State the blood parasite species.
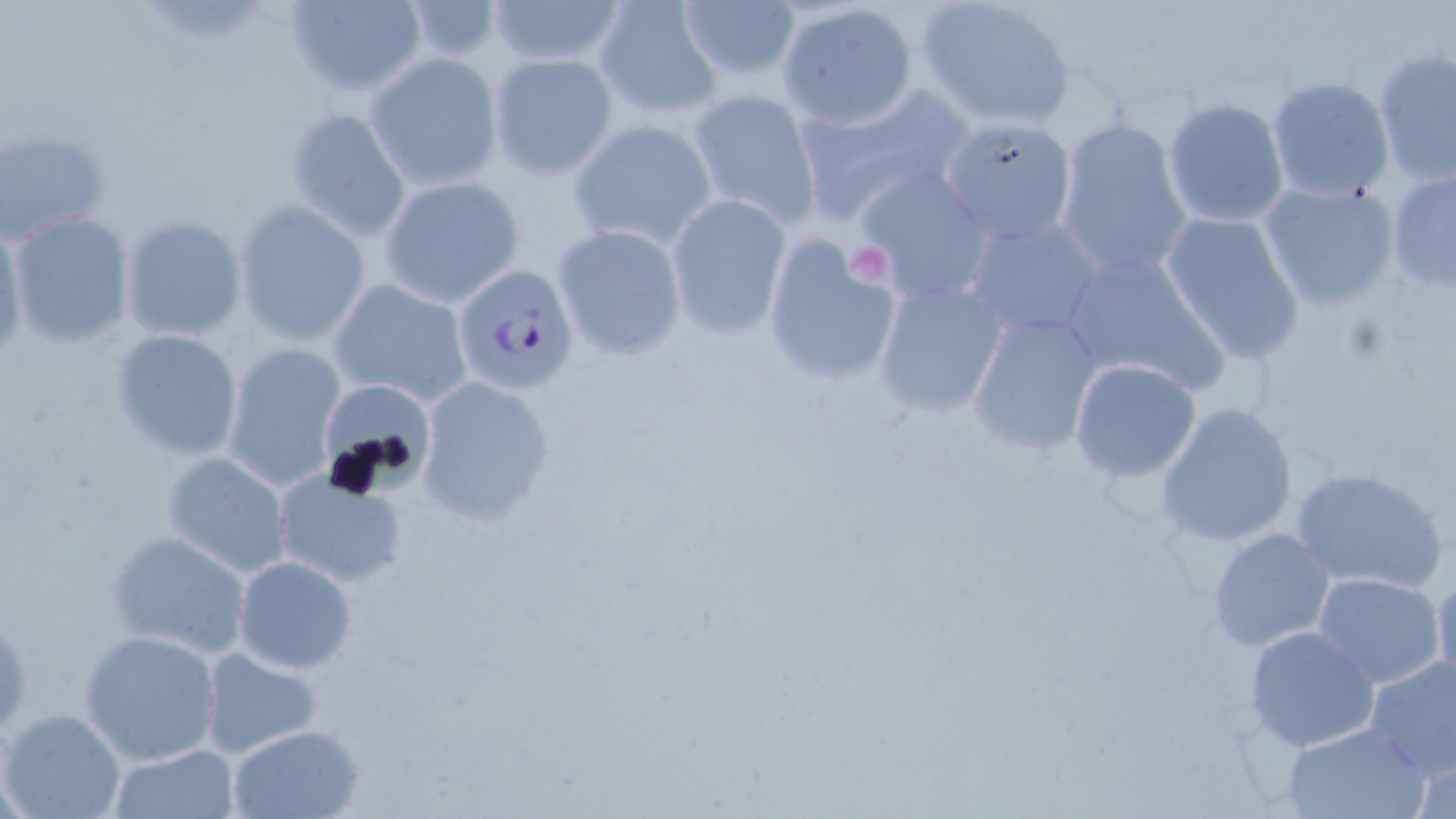

Plasmodium falciparum.

image size = 1456×819 pixels
uninfected red blood cell locations = approximate bounding boxes as [x1, y1, x2, y2] in pixels: [284, 0, 428, 99], [488, 0, 622, 69], [594, 0, 724, 121], [679, 0, 803, 84], [917, 0, 1077, 129], [401, 1, 505, 62], [778, 3, 920, 129], [1372, 50, 1456, 187], [490, 53, 619, 178], [365, 54, 503, 191], [1266, 76, 1395, 202], [791, 83, 973, 226], [687, 88, 821, 226], [1162, 99, 1292, 228], [286, 106, 410, 241], [940, 116, 1077, 245], [1054, 117, 1194, 280], [567, 119, 718, 251], [1, 128, 112, 244], [853, 166, 993, 303], [1386, 168, 1456, 292], [379, 177, 524, 306], [1259, 181, 1399, 311], [667, 194, 791, 337], [234, 201, 370, 345], [8, 211, 135, 348], [1160, 211, 1307, 363], [963, 214, 1107, 342], [119, 215, 248, 342], [0, 219, 28, 367], [553, 225, 687, 359], [760, 233, 903, 387], [1059, 249, 1230, 396], [327, 276, 474, 408], [872, 277, 1008, 417], [966, 313, 1105, 456], [111, 329, 243, 462], [221, 342, 344, 489], [1068, 359, 1202, 482], [415, 375, 558, 524], [321, 382, 432, 485], [1156, 402, 1298, 547], [161, 452, 291, 576], [1290, 465, 1448, 594], [271, 470, 409, 589], [1207, 526, 1335, 651], [105, 527, 253, 659], [233, 555, 357, 673], [1433, 568, 1456, 690], [1311, 571, 1447, 690], [1243, 625, 1382, 753], [79, 628, 223, 765], [197, 648, 324, 759], [1363, 655, 1456, 779], [1, 707, 126, 819], [1281, 721, 1430, 819], [225, 723, 365, 818], [106, 744, 240, 818], [1411, 753, 1456, 819]
stain = May-Grünwald-Giemsa
preparation = thin blood film
platelet locations = approximate bounding boxes as [x1, y1, x2, y2] in pixels: [849, 241, 893, 283]
modality = optical microscopy
field of view = one of a larger specimen
Plasmodium falciparum-infected red blood cell locations = approximate bounding boxes as [x1, y1, x2, y2] in pixels: [451, 263, 581, 393]
magnification = 1000x